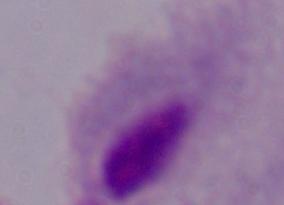
modality: micrograph
identification: trichomonad
magnification: 1000x